State the blood parasite species.
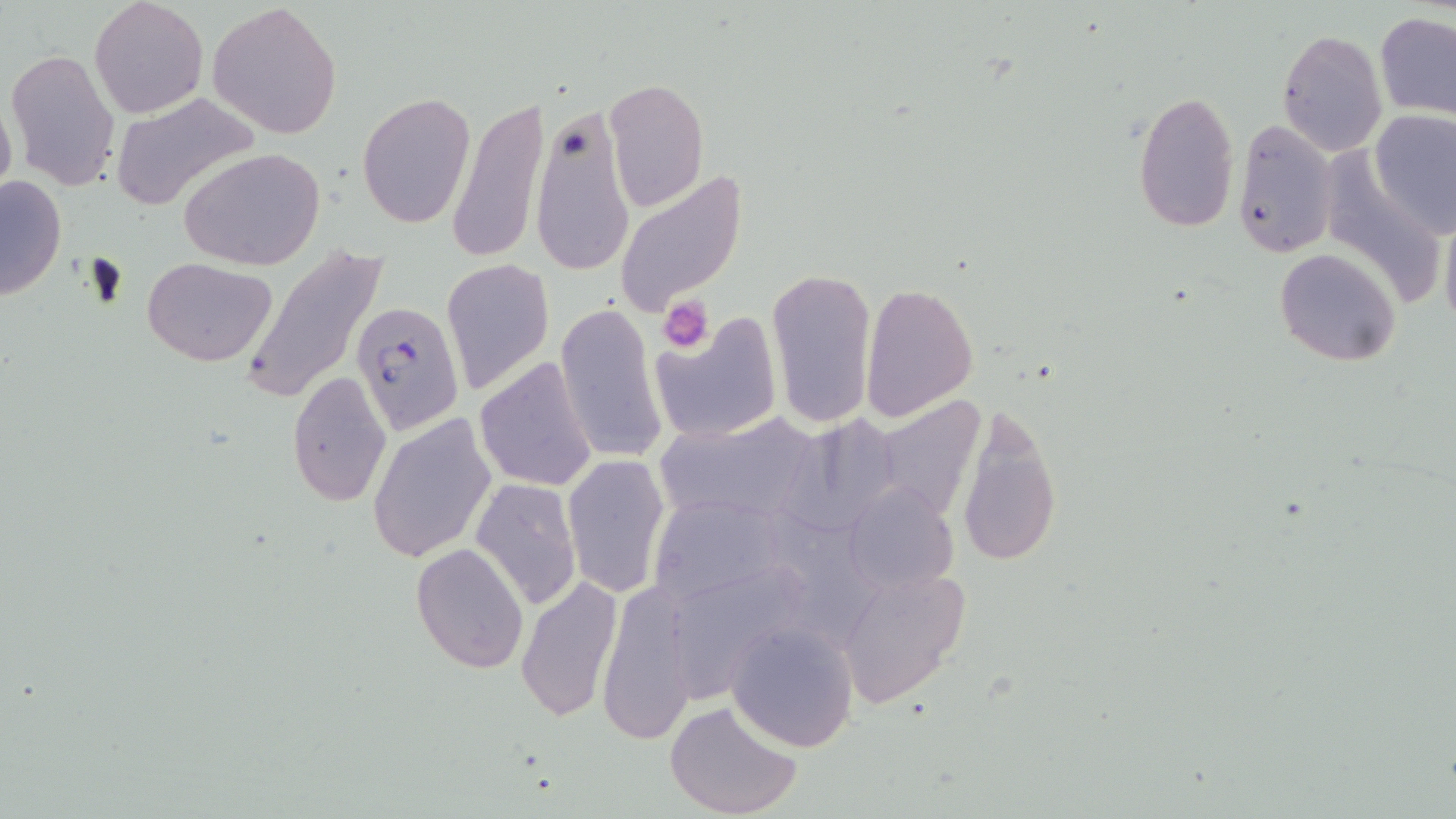
Plasmodium falciparum.

Approximate bounding boxes as [x1, y1, x2, y2] in pixels. Plasmodium falciparum-infected red blood cell locations: [351, 299, 463, 435]. Platelet locations: [661, 298, 714, 351]. Uninfected red blood cell locations: [89, 0, 209, 119], [208, 2, 345, 139], [1376, 14, 1456, 119], [1277, 29, 1388, 156], [6, 47, 121, 193], [604, 76, 709, 213], [110, 91, 260, 211], [1133, 91, 1240, 233], [356, 92, 476, 230], [0, 93, 17, 205], [447, 97, 549, 265], [528, 99, 636, 279], [1370, 108, 1456, 236], [1232, 117, 1338, 260], [178, 147, 327, 271], [613, 168, 749, 316], [0, 174, 67, 302], [1439, 204, 1456, 342], [244, 243, 390, 407], [1274, 249, 1401, 367], [142, 257, 276, 367], [440, 259, 555, 395], [766, 265, 878, 426], [859, 282, 979, 421], [554, 302, 668, 465], [649, 313, 784, 444], [474, 357, 599, 490], [288, 371, 392, 506], [873, 395, 988, 524], [958, 409, 1059, 569], [366, 412, 497, 566], [655, 413, 822, 524], [561, 454, 670, 598], [470, 477, 582, 612], [840, 483, 957, 597], [646, 493, 792, 609], [768, 509, 887, 647], [410, 542, 529, 672], [834, 567, 965, 705], [514, 575, 622, 723], [596, 582, 699, 746], [726, 620, 860, 753], [664, 700, 803, 819]. Thin blood film. 1000x magnification. One field of a larger specimen. Light microscopy. May-Grünwald-Giemsa-stained preparation. Image is 1456×819 pixels.